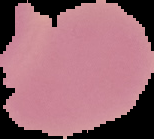
image size = 154×139 pixels
image type = cell region segmented out of the field of view; surrounding area masked to black
preparation = thin blood film
malaria status = uninfected